Locate malaria parasites and leukocytes.
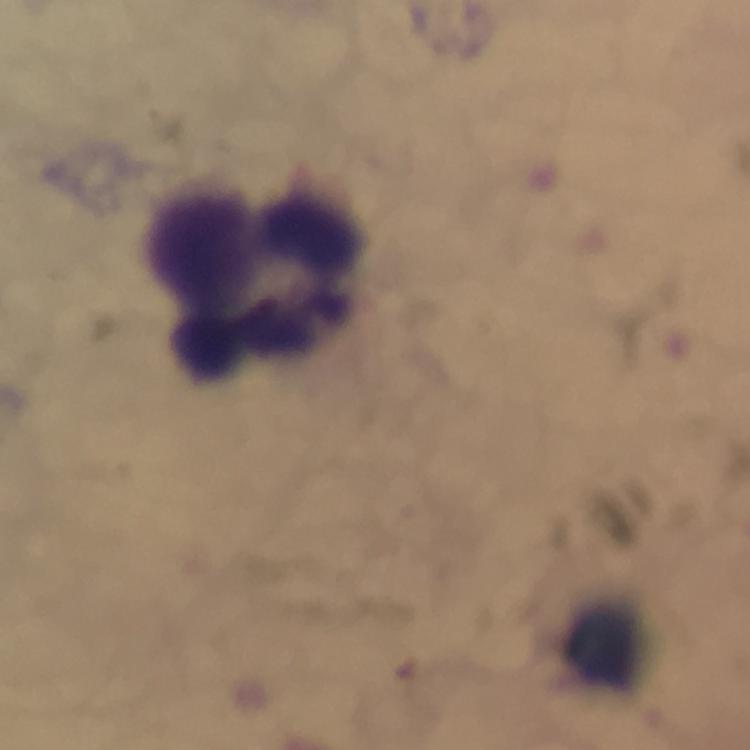
No malaria parasites detected.
Approximate centers as [x, y] in pixels.
Leukocytes: [257, 286], [603, 645].

Summary:
  - Context: from a malaria diagnostic workup
  - Preparation: thick blood smear
  - Magnification: 100x
  - Capture: smartphone camera through the microscope
  - Stain: Giemsa
  - Cropped from: a single field of view
  - Immersion oil: used
  - Image size: 750×750 pixels